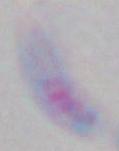

Toxoplasma gondii is seen. Captured at 1000x magnification. Photomicrograph.